State which parasite is depicted.
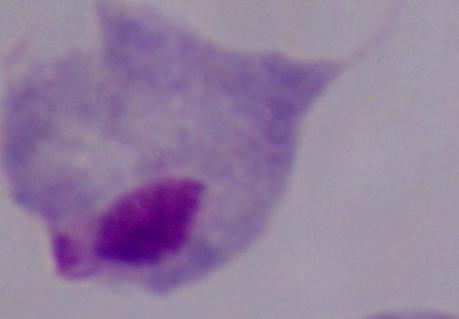
A trichomonad.

Summary:
  - Modality: photomicrograph
  - Magnification: 1000x